Name the parasite shown.
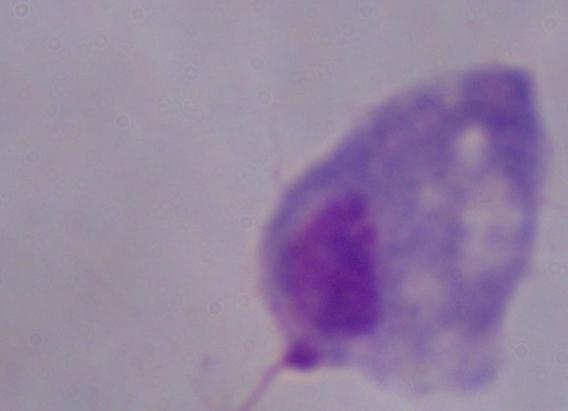

A trichomonad.

magnification = 1000x
modality = photomicrograph